Point out each Plasmodium parasite.
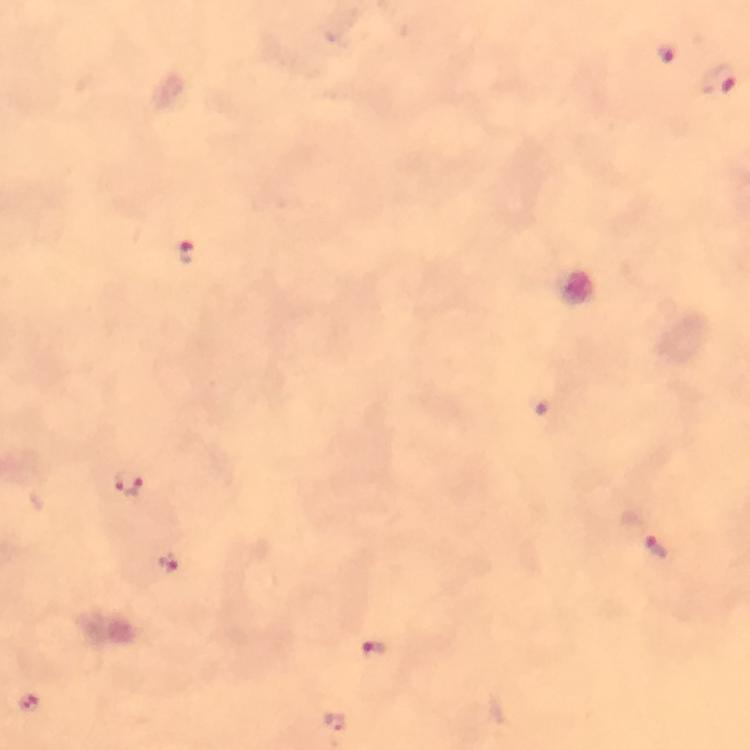
Approximate centers as (x, y) in pixels.
Plasmodium parasites: (663, 53), (719, 79), (186, 248), (128, 484), (658, 546), (168, 563), (376, 651), (30, 701).

cropped from = a single field of view
preparation = thick blood film
magnification = 100x
context = from a malaria diagnostic workup
capture = smartphone mounted on the microscope
stain = Giemsa
image size = 750×750 pixels
immersion oil = used